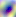

Summary:
  - Identification: Toxoplasma gondii
  - Modality: micrograph
  - Magnification: 400x